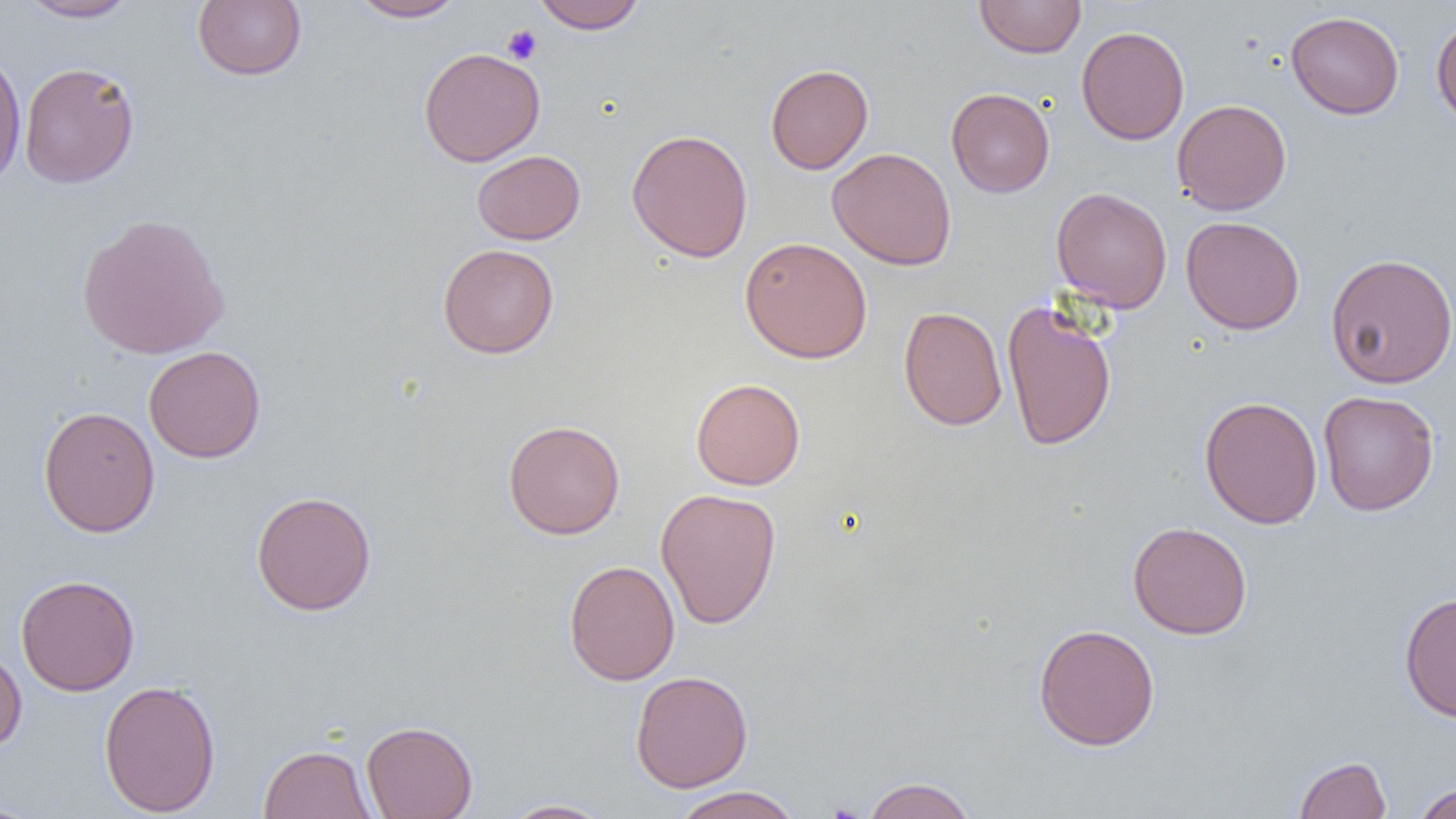
Summary:
  - Coordinate format: approximate bounding boxes as [x1, y1, x2, y2] in pixels
  - Platelet locations: [503, 25, 542, 65]
  - Uninfected red blood cell locations: [17, 0, 140, 22], [348, 0, 466, 22], [974, 0, 1086, 58], [193, 1, 307, 81], [531, 1, 647, 33], [1286, 11, 1404, 119], [1431, 15, 1456, 127], [1076, 25, 1189, 145], [0, 46, 27, 191], [418, 47, 545, 167], [18, 61, 140, 188], [765, 63, 874, 174], [946, 87, 1055, 197], [1172, 99, 1292, 215], [626, 128, 753, 263], [827, 147, 957, 270], [472, 150, 585, 245], [1051, 187, 1172, 312], [76, 213, 230, 359], [1181, 216, 1305, 334], [740, 236, 872, 364], [438, 244, 559, 358], [1325, 253, 1456, 388], [1002, 299, 1117, 452], [898, 306, 1008, 431], [143, 345, 266, 463], [690, 378, 806, 490], [1318, 390, 1439, 516], [1199, 395, 1322, 529], [38, 405, 160, 538], [503, 420, 625, 540], [655, 487, 782, 629], [251, 490, 377, 616], [1128, 521, 1252, 639], [564, 559, 680, 686], [15, 574, 140, 696], [1399, 591, 1456, 723], [1033, 623, 1160, 750], [0, 648, 27, 752], [631, 670, 753, 792], [99, 679, 221, 817], [361, 720, 478, 819], [258, 744, 375, 819], [1294, 756, 1391, 818], [862, 776, 976, 819], [1413, 782, 1456, 819], [671, 786, 803, 819], [500, 799, 613, 818], [0, 800, 44, 819]
  - Slide-level diagnosis: no evidence of blood parasites
  - Magnification: 1000x
  - Image size: 1456×819 pixels
  - Field of view: one of a larger specimen
  - Modality: light microscopy
  - Preparation: thin blood smear